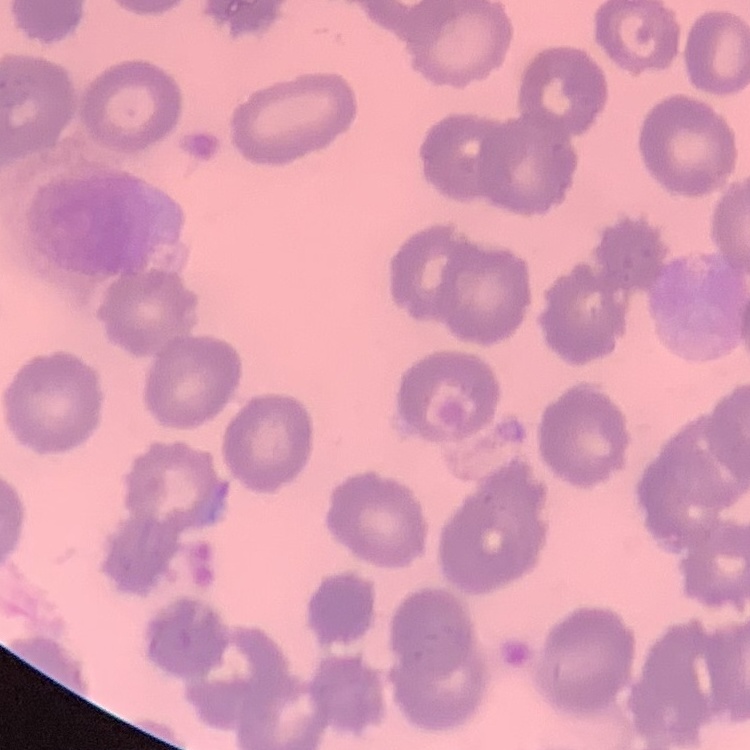
The erythrocytes show no rouleaux formation. Thin blood film. One tile cut from a larger photomicrograph. Stained with either Field's or Giemsa.